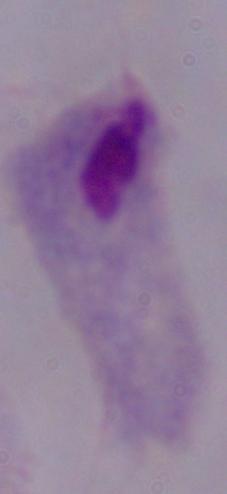

magnification = 1000x
modality = micrograph
identification = trichomonad